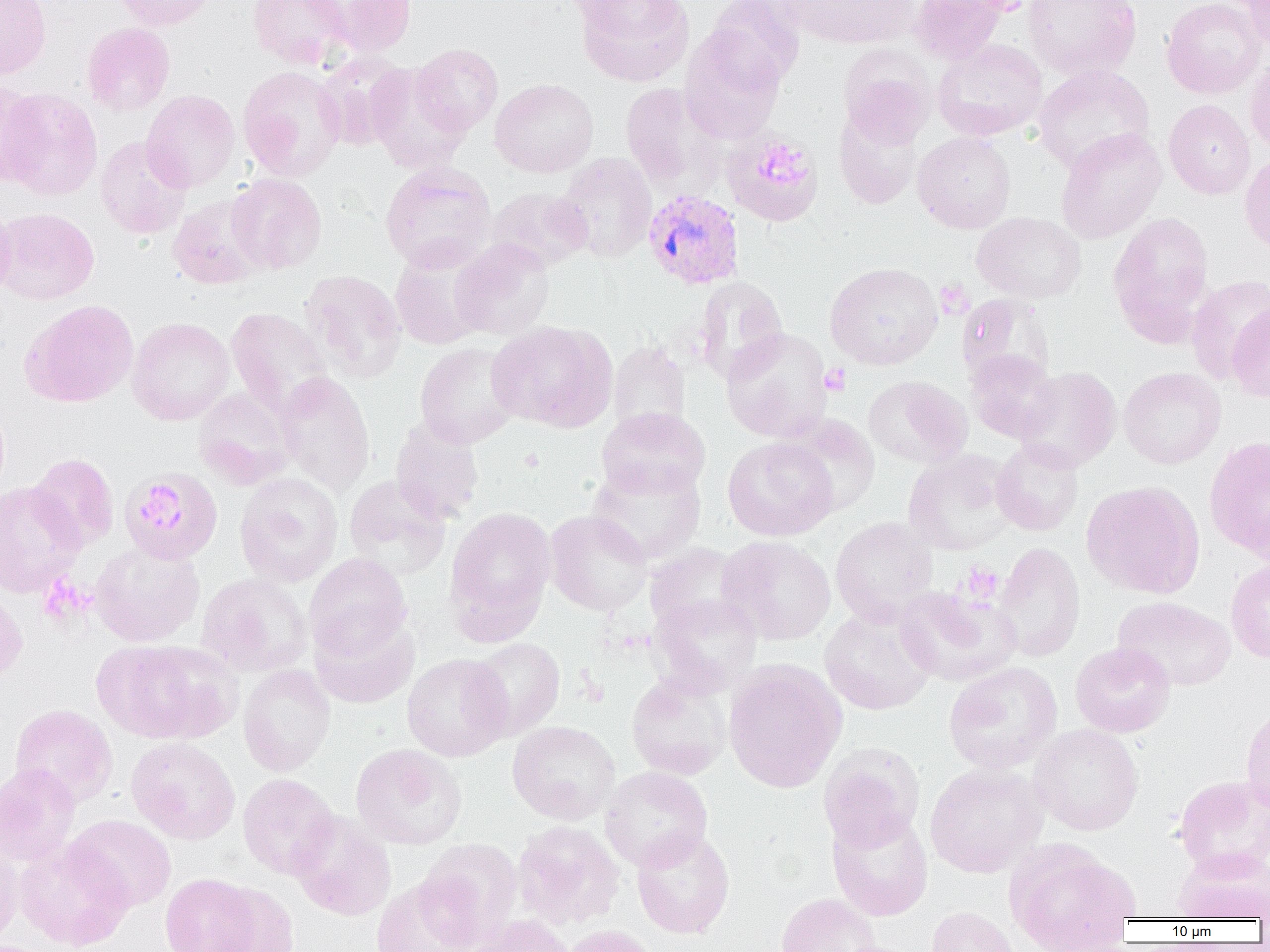 Approximate bounding boxes as named x1/y1/x2/y2 corners in pixels. Uninfected red blood cell locations: (x1=0, y1=0, x2=52, y2=80), (x1=112, y1=0, x2=216, y2=30), (x1=247, y1=0, x2=352, y2=70), (x1=313, y1=0, x2=418, y2=56), (x1=574, y1=0, x2=694, y2=87), (x1=706, y1=0, x2=805, y2=88), (x1=778, y1=0, x2=919, y2=49), (x1=909, y1=0, x2=1008, y2=64), (x1=947, y1=0, x2=1040, y2=16), (x1=1022, y1=0, x2=1142, y2=81), (x1=1161, y1=0, x2=1265, y2=99), (x1=1241, y1=0, x2=1270, y2=54), (x1=82, y1=22, x2=175, y2=116), (x1=680, y1=25, x2=787, y2=143), (x1=931, y1=39, x2=1048, y2=141), (x1=410, y1=44, x2=504, y2=135), (x1=840, y1=48, x2=936, y2=150), (x1=315, y1=52, x2=411, y2=150), (x1=1245, y1=58, x2=1270, y2=153), (x1=1032, y1=64, x2=1156, y2=173), (x1=366, y1=65, x2=471, y2=174), (x1=238, y1=66, x2=346, y2=181), (x1=490, y1=78, x2=599, y2=177), (x1=0, y1=81, x2=43, y2=187), (x1=620, y1=83, x2=726, y2=194), (x1=1, y1=88, x2=102, y2=201), (x1=141, y1=90, x2=240, y2=193), (x1=1164, y1=99, x2=1255, y2=199), (x1=834, y1=105, x2=923, y2=210), (x1=834, y1=116, x2=1012, y2=216), (x1=1055, y1=128, x2=1166, y2=244), (x1=723, y1=131, x2=823, y2=226), (x1=913, y1=131, x2=1016, y2=234), (x1=95, y1=136, x2=192, y2=239), (x1=556, y1=152, x2=657, y2=263), (x1=1240, y1=152, x2=1270, y2=257), (x1=380, y1=162, x2=496, y2=272), (x1=226, y1=173, x2=327, y2=274), (x1=487, y1=186, x2=593, y2=272), (x1=0, y1=194, x2=17, y2=303), (x1=168, y1=195, x2=269, y2=289), (x1=0, y1=207, x2=99, y2=304), (x1=1108, y1=211, x2=1215, y2=343), (x1=972, y1=212, x2=1086, y2=303), (x1=450, y1=238, x2=554, y2=341), (x1=389, y1=243, x2=493, y2=350), (x1=825, y1=261, x2=943, y2=370), (x1=300, y1=270, x2=406, y2=383), (x1=1186, y1=274, x2=1270, y2=384), (x1=692, y1=276, x2=789, y2=383), (x1=957, y1=294, x2=1056, y2=389), (x1=20, y1=299, x2=139, y2=407), (x1=1228, y1=303, x2=1270, y2=403), (x1=226, y1=307, x2=334, y2=419), (x1=127, y1=317, x2=235, y2=425), (x1=487, y1=320, x2=618, y2=432), (x1=721, y1=327, x2=832, y2=443), (x1=608, y1=340, x2=691, y2=438), (x1=414, y1=342, x2=522, y2=448), (x1=966, y1=350, x2=1060, y2=443), (x1=1015, y1=366, x2=1122, y2=472), (x1=1118, y1=367, x2=1226, y2=469), (x1=275, y1=371, x2=376, y2=495), (x1=863, y1=375, x2=972, y2=469), (x1=192, y1=387, x2=297, y2=489), (x1=596, y1=407, x2=711, y2=499), (x1=781, y1=414, x2=882, y2=516), (x1=390, y1=418, x2=485, y2=524), (x1=722, y1=435, x2=839, y2=541), (x1=1204, y1=435, x2=1270, y2=561), (x1=991, y1=439, x2=1084, y2=536), (x1=902, y1=449, x2=1018, y2=555), (x1=28, y1=453, x2=119, y2=551), (x1=587, y1=461, x2=707, y2=565), (x1=119, y1=467, x2=223, y2=566), (x1=234, y1=472, x2=344, y2=587), (x1=343, y1=475, x2=452, y2=580), (x1=0, y1=480, x2=85, y2=597), (x1=1082, y1=480, x2=1205, y2=598), (x1=444, y1=507, x2=556, y2=637), (x1=544, y1=510, x2=652, y2=615), (x1=830, y1=516, x2=939, y2=625), (x1=716, y1=535, x2=836, y2=645), (x1=992, y1=541, x2=1085, y2=663), (x1=89, y1=542, x2=205, y2=646), (x1=644, y1=544, x2=749, y2=635), (x1=304, y1=553, x2=412, y2=661), (x1=1226, y1=559, x2=1270, y2=663), (x1=196, y1=572, x2=313, y2=677), (x1=218, y1=572, x2=321, y2=767), (x1=893, y1=585, x2=1020, y2=686), (x1=0, y1=590, x2=27, y2=686), (x1=649, y1=593, x2=763, y2=695), (x1=1112, y1=596, x2=1236, y2=691), (x1=819, y1=605, x2=938, y2=715), (x1=310, y1=611, x2=420, y2=709), (x1=468, y1=637, x2=565, y2=739), (x1=92, y1=639, x2=232, y2=743), (x1=1070, y1=641, x2=1176, y2=738), (x1=402, y1=653, x2=513, y2=761), (x1=723, y1=660, x2=847, y2=793), (x1=943, y1=661, x2=1063, y2=775), (x1=238, y1=665, x2=336, y2=776), (x1=625, y1=671, x2=733, y2=779), (x1=9, y1=704, x2=118, y2=806), (x1=1240, y1=706, x2=1270, y2=813), (x1=507, y1=721, x2=620, y2=824), (x1=1029, y1=723, x2=1144, y2=836), (x1=127, y1=737, x2=240, y2=843), (x1=350, y1=743, x2=467, y2=850), (x1=819, y1=743, x2=924, y2=851), (x1=0, y1=762, x2=81, y2=866), (x1=924, y1=762, x2=1048, y2=878), (x1=600, y1=766, x2=713, y2=871), (x1=238, y1=773, x2=339, y2=880), (x1=1173, y1=773, x2=1270, y2=877), (x1=827, y1=810, x2=933, y2=921), (x1=290, y1=812, x2=396, y2=921), (x1=65, y1=814, x2=177, y2=912), (x1=512, y1=820, x2=624, y2=930), (x1=631, y1=829, x2=735, y2=939), (x1=0, y1=838, x2=23, y2=946), (x1=416, y1=838, x2=523, y2=948), (x1=14, y1=839, x2=134, y2=950), (x1=1004, y1=839, x2=1140, y2=952), (x1=1172, y1=849, x2=1270, y2=922), (x1=160, y1=873, x2=262, y2=952), (x1=371, y1=877, x2=480, y2=952), (x1=207, y1=884, x2=299, y2=952), (x1=776, y1=893, x2=881, y2=952), (x1=926, y1=906, x2=1020, y2=952), (x1=470, y1=915, x2=576, y2=952), (x1=559, y1=925, x2=660, y2=952). Plasmodium vivax-infected red blood cell locations: (x1=643, y1=189, x2=745, y2=291). Platelet locations: (x1=756, y1=147, x2=812, y2=186), (x1=935, y1=281, x2=973, y2=318), (x1=820, y1=363, x2=851, y2=396), (x1=134, y1=488, x2=188, y2=534), (x1=961, y1=563, x2=1003, y2=603), (x1=38, y1=573, x2=96, y2=628). Slide-level diagnosis: Plasmodium vivax. Image is 1270×952 pixels. Light microscopy. Thin blood smear. Captured at 1000x magnification. One field of a larger specimen.